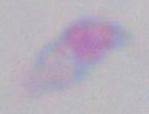 Photomicrograph. Captured at 1000x magnification. Toxoplasma gondii is seen.